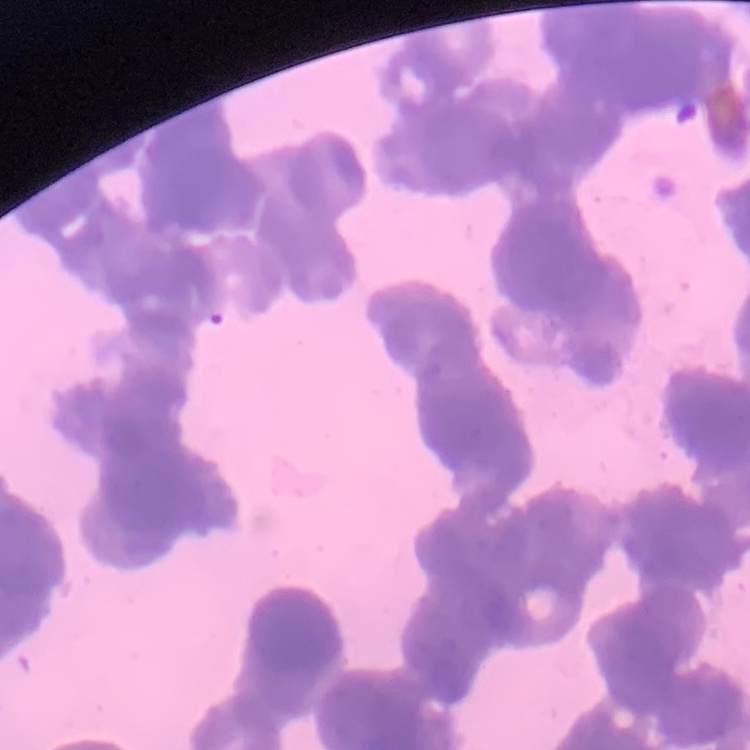
Summary:
  - Red blood cell morphology: rouleaux formation
  - Stain: Field's or Giemsa
  - Preparation: thin blood smear
  - Image type: square crop of a larger photomicrograph